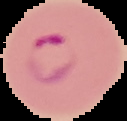

Summary:
  - Image size: 127×121 pixels
  - Malaria status: parasitized
  - Image type: segmented cell region on a black background
  - Preparation: thin blood film